Name the blood parasite species.
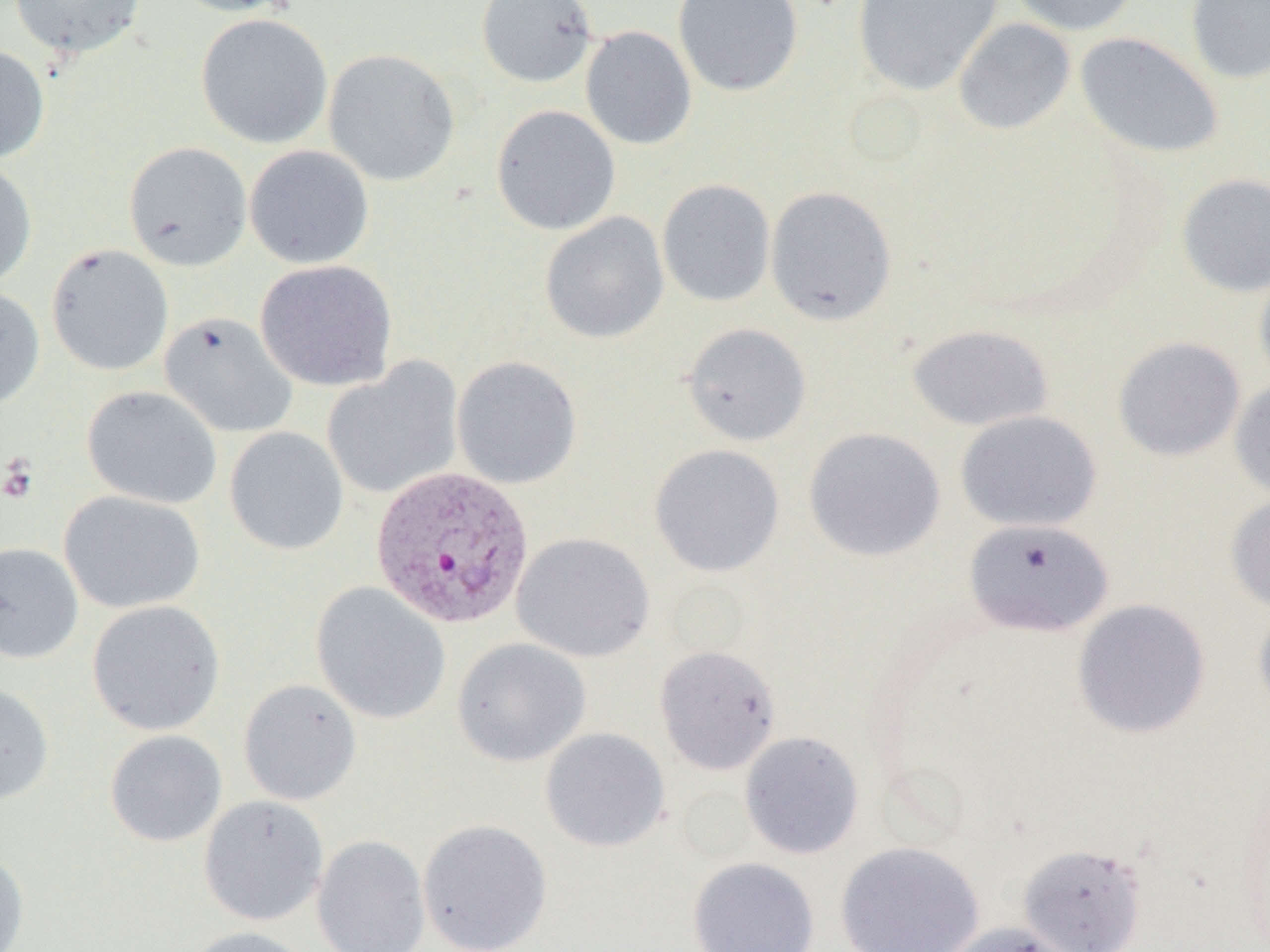
Plasmodium vivax.

image size = 1270×952 pixels
Plasmodium vivax-infected red blood cell locations = approximate bounding boxes as (x1, y1, x2, y2) in pixels: (370, 464, 536, 630)
preparation = thin blood film
magnification = 1000x
platelet locations = approximate bounding boxes as (x1, y1, x2, y2) in pixels: (1, 457, 38, 504)
modality = optical microscopy
uninfected red blood cell locations = approximate bounding boxes as (x1, y1, x2, y2) in pixels: (8, 0, 146, 58), (166, 0, 302, 17), (476, 0, 597, 88), (672, 0, 803, 97), (852, 0, 1002, 96), (1008, 0, 1139, 36), (1185, 0, 1270, 84), (195, 12, 333, 149), (953, 18, 1076, 135), (580, 25, 697, 150), (1075, 32, 1223, 159), (0, 45, 50, 163), (322, 47, 460, 187), (491, 104, 621, 236), (122, 141, 252, 272), (244, 145, 374, 269), (0, 158, 37, 290), (1176, 174, 1270, 297), (657, 179, 776, 307), (765, 185, 897, 326), (539, 212, 670, 344), (46, 243, 174, 376), (254, 260, 397, 391), (1254, 264, 1270, 389), (0, 285, 46, 409), (159, 312, 298, 438), (681, 322, 812, 446), (906, 324, 1054, 432), (1113, 336, 1246, 461), (451, 355, 583, 489), (321, 359, 464, 501), (1230, 379, 1270, 501), (81, 385, 223, 509), (955, 410, 1103, 533), (224, 427, 349, 555), (803, 427, 946, 563), (648, 443, 786, 577), (59, 490, 205, 614), (1225, 493, 1270, 613), (963, 518, 1114, 638), (512, 532, 655, 662), (0, 542, 83, 664), (311, 582, 451, 725), (1253, 598, 1270, 720), (1072, 599, 1211, 739), (86, 600, 226, 736), (452, 638, 591, 767), (654, 644, 782, 775), (238, 678, 361, 806), (0, 682, 54, 805), (539, 727, 670, 852), (104, 729, 227, 847), (739, 731, 864, 859), (198, 795, 329, 927), (417, 818, 553, 952), (311, 834, 431, 952), (835, 840, 985, 952), (1017, 843, 1147, 951), (0, 847, 30, 952), (687, 857, 820, 952), (940, 921, 1081, 952), (181, 925, 318, 952)
field of view = single